Assess this cell for malaria.
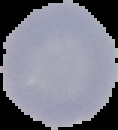

Uninfected.

From a thin blood film. Image is 118×130 pixels. The area outside the segmented cell region is set to black.